Classify this cell by malaria status.
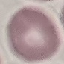

It is uninfected.

Thin blood film. Giemsa stain. Automatically extracted cell patch, resized to 64 × 64 pixels. Acquired by smartphone through the microscope eyepiece.